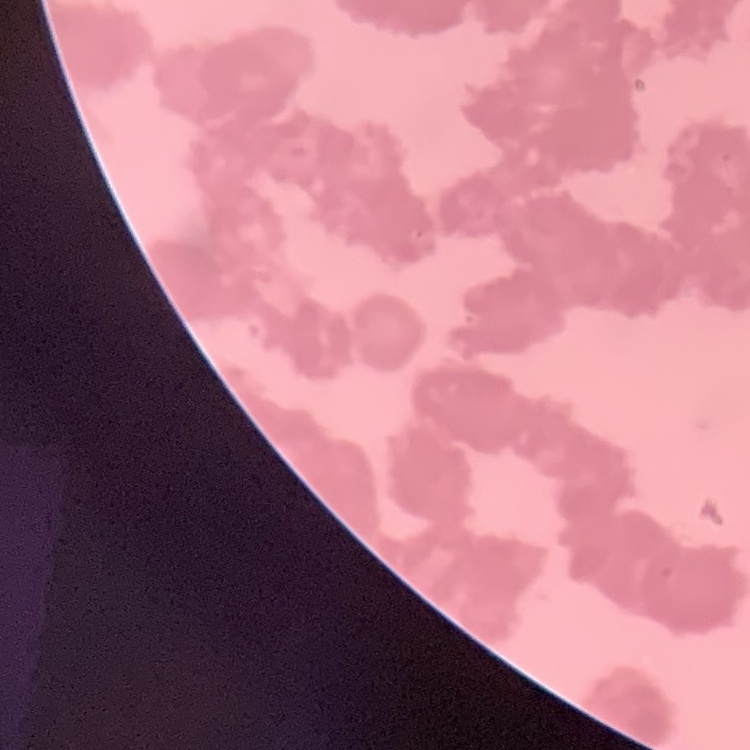
{
  "erythrocyte_morphology": "rouleaux formation",
  "image_type": "one tile cut from a larger photomicrograph",
  "stain": "Field's or Giemsa",
  "preparation": "thin peripheral smear"
}